Describe the morphology of the erythrocytes.
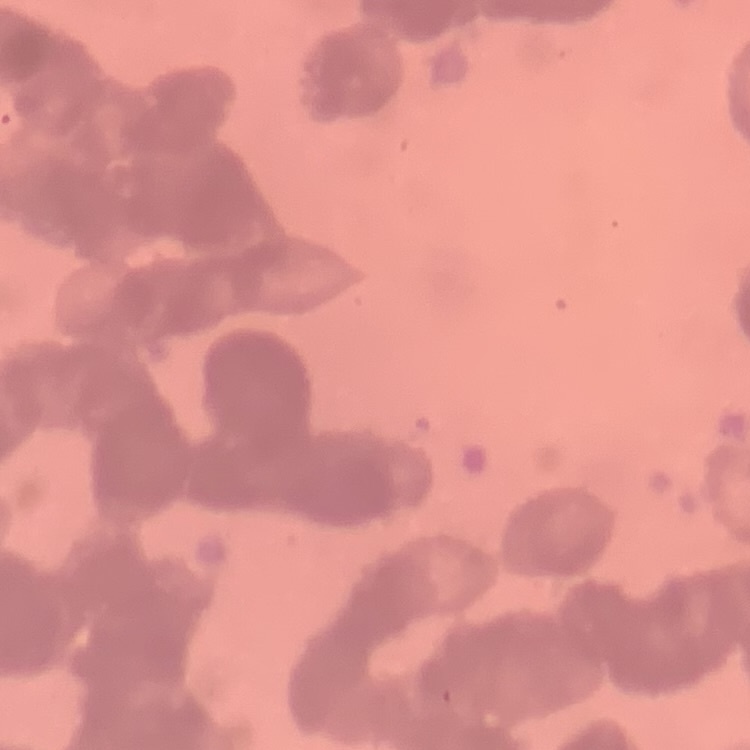
Rouleaux formation.

Stained with either Field's or Giemsa. Square crop of a larger photomicrograph. Thin peripheral smear.